State the blood parasite species.
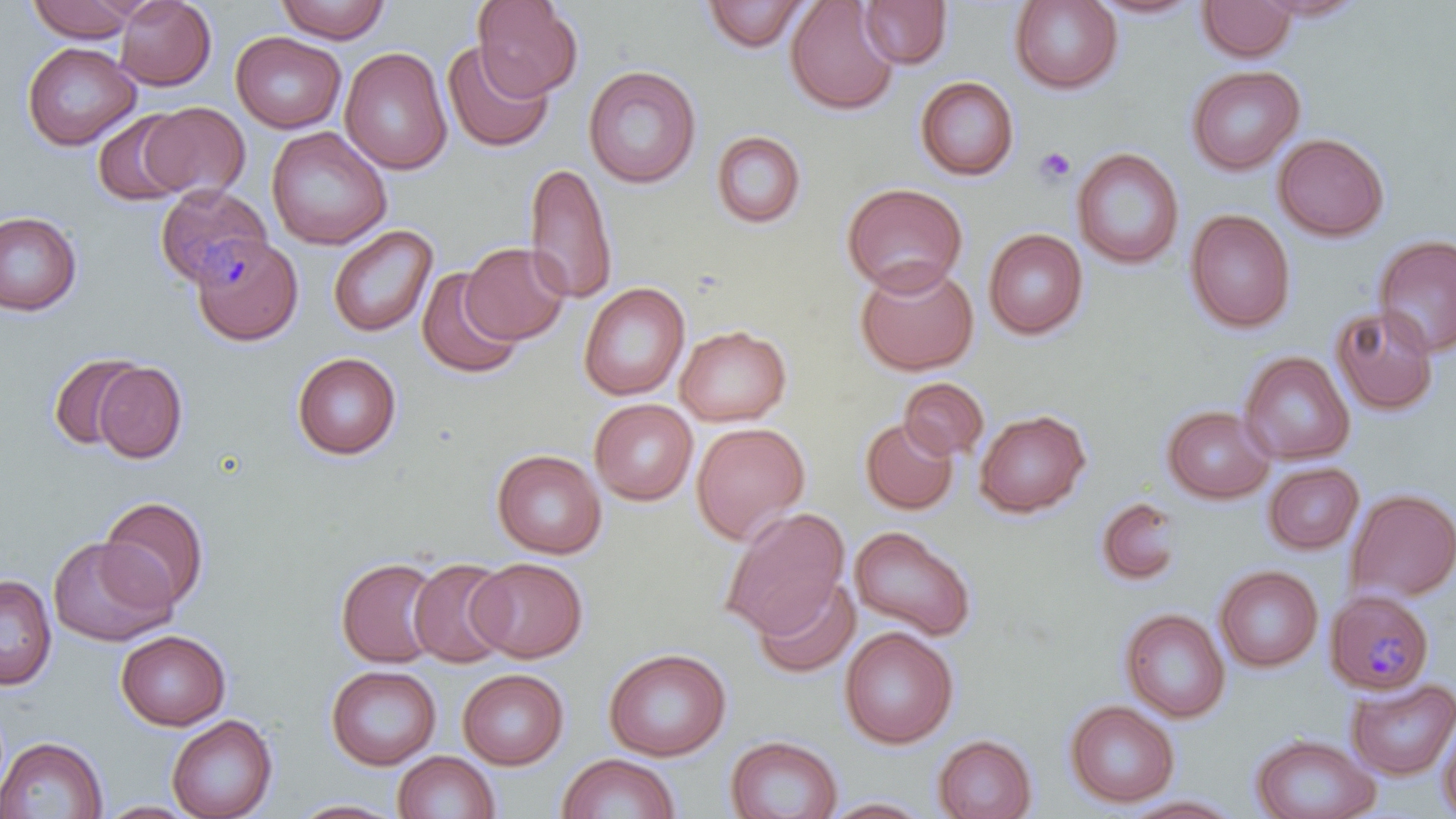

Plasmodium malariae.

uninfected red blood cell locations = approximate bounding boxes as (x1,y1)-(x2,y2) corner pairs in pixels: (26,0)-(140,43), (114,0)-(216,90), (273,0)-(391,43), (472,0)-(583,99), (783,0)-(901,116), (1009,0)-(1123,94), (1088,0)-(1207,20), (1251,0)-(1370,22), (701,1)-(810,52), (857,1)-(952,69), (1197,1)-(1297,62), (231,32)-(346,133), (230,39)-(457,146), (22,42)-(140,151), (441,42)-(554,153), (339,47)-(452,175), (1186,64)-(1305,176), (583,65)-(701,189), (915,76)-(1019,181), (138,101)-(251,200), (92,110)-(192,206), (266,126)-(392,250), (710,130)-(808,229), (1272,131)-(1390,242), (1071,147)-(1185,270), (524,161)-(618,306), (842,182)-(968,296), (1185,209)-(1296,333), (0,211)-(82,316), (327,224)-(438,337), (983,228)-(1088,340), (1373,233)-(1456,357), (190,235)-(302,346), (460,242)-(571,345), (854,261)-(979,376), (416,267)-(524,379), (578,282)-(690,401), (1330,305)-(1439,416), (675,324)-(792,426), (49,349)-(147,454), (1239,350)-(1355,465), (291,352)-(402,460), (94,362)-(187,463), (899,377)-(989,461), (589,399)-(698,505), (1161,404)-(1275,504), (974,409)-(1091,518), (860,417)-(958,514), (690,422)-(811,545), (492,449)-(607,559), (1263,462)-(1364,554), (1344,488)-(1456,603), (1093,495)-(1185,589), (97,496)-(211,612), (720,506)-(851,639), (848,525)-(977,641), (47,537)-(176,647), (336,557)-(443,668), (468,557)-(588,662), (408,558)-(513,668), (1215,565)-(1323,673), (0,574)-(57,690), (753,577)-(860,679), (1120,608)-(1230,722), (839,626)-(958,749), (115,630)-(231,731), (603,647)-(732,761), (325,664)-(441,770), (457,668)-(569,769), (1346,677)-(1456,780), (1064,700)-(1179,808), (1437,713)-(1456,819), (166,715)-(278,819), (1250,733)-(1380,819), (726,734)-(843,819), (932,734)-(1037,819), (0,736)-(108,818), (393,751)-(500,819), (556,753)-(681,818), (1120,794)-(1245,818), (822,796)-(933,818), (287,798)-(407,818), (94,800)-(204,818)
platelet locations = approximate bounding boxes as (x1,y1)-(x2,y2) corner pairs in pixels: (1034,146)-(1077,186)
image size = 1456×819 pixels
field of view = one of a larger specimen
magnification = 1000x
preparation = thin blood film
modality = optical microscopy
stain = May-Grünwald-Giemsa
Plasmodium malariae-infected red blood cell locations = approximate bounding boxes as (x1,y1)-(x2,y2) corner pairs in pixels: (154,184)-(272,290), (1325,591)-(1436,701)